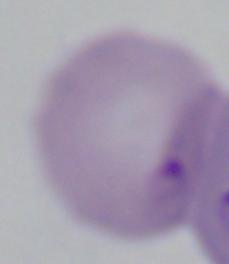

1000x magnification. Micrograph. A Babesia parasite is shown.